State the preparation type.
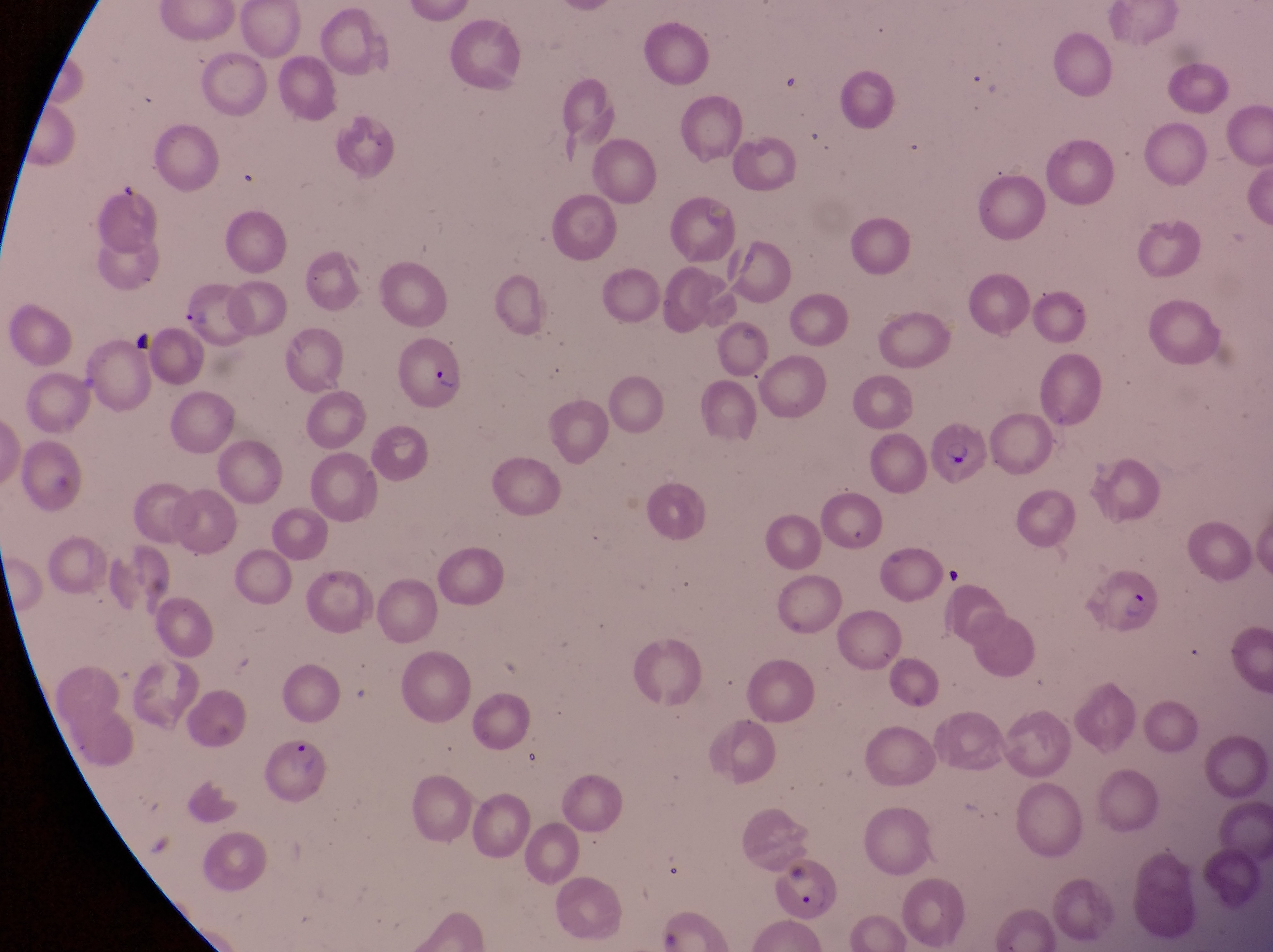

This is a thin smear.

parasitised red blood cell locations = approximate bounding boxes as (left, top, right, bottom) in pixels: (178, 289, 257, 350), (397, 337, 469, 407), (924, 422, 984, 487), (1091, 567, 1161, 639), (264, 732, 333, 809), (771, 859, 845, 924)
image size = 1273×952 pixels
country = Uganda
artifact (platelet-like body, stain precipitate, or debris) locations = approximate bounding boxes as (left, top, right, bottom) in pixels: (127, 327, 164, 362), (938, 559, 968, 598)
field of view = single
capture = smartphone photograph through the eyepiece of an Olympus CX-23 microscope
magnification = 1000x